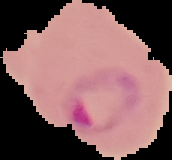
{
  "preparation": "thin blood smear",
  "result": "malaria parasites detected",
  "image_type": "segmented cell region with the area outside set to black",
  "image_size": "172×160 pixels"
}